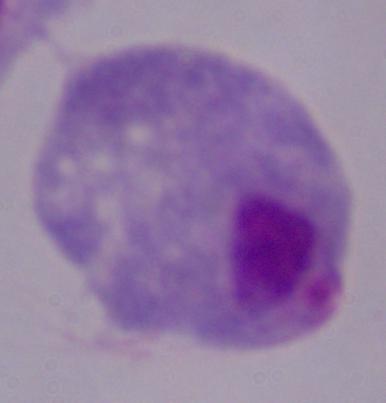

Summary:
  - Identification: trichomonad
  - Magnification: 1000x
  - Modality: micrograph